Point out each leukocyte.
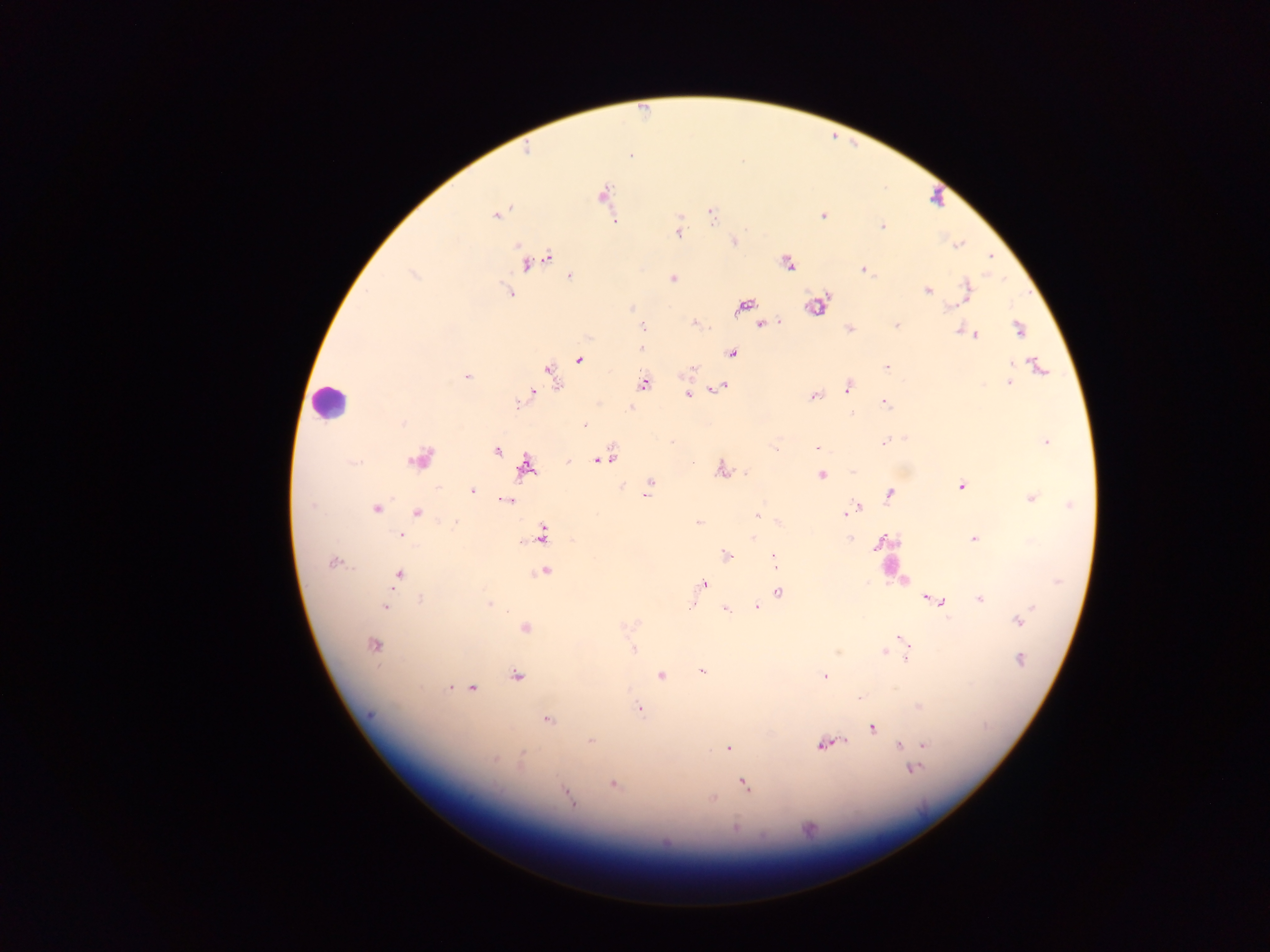
Approximate centers as [x, y] in pixels.
Leukocytes: [328, 403].

field of view = single
image size = 1270×952 pixels
capture = mobile-phone photograph through a microscope
malaria parasite locations = approximate centers as [x, y] in pixels: [630, 154], [603, 195], [711, 214], [821, 215], [496, 217], [679, 221], [882, 226], [677, 230], [734, 242], [548, 258], [787, 262], [526, 266], [863, 270], [569, 275], [672, 278], [506, 284], [966, 284], [928, 291], [510, 292], [967, 296], [963, 300], [948, 304], [631, 306], [781, 320], [693, 322], [643, 325], [760, 325], [896, 325], [849, 328], [961, 328], [1017, 328], [976, 336], [641, 348], [733, 354], [579, 359], [1012, 364], [1036, 366], [885, 367], [694, 370], [549, 371], [467, 376], [644, 384], [1009, 384], [723, 386], [982, 386], [713, 390], [846, 390], [534, 392], [688, 393], [813, 396], [884, 403], [517, 404], [630, 408], [402, 424], [583, 424], [905, 438], [884, 440], [1044, 440], [672, 441], [817, 448], [498, 452], [610, 457], [419, 458], [599, 458], [566, 463], [691, 463], [527, 468], [722, 468], [851, 471], [820, 474], [650, 484], [961, 485], [623, 486], [471, 491], [888, 493], [646, 494], [1031, 497], [507, 501], [1071, 505], [859, 507], [376, 509], [851, 509], [756, 513], [418, 514], [845, 515], [454, 521], [697, 521], [544, 534], [401, 535], [751, 536], [849, 537], [972, 538], [881, 540], [520, 542], [725, 555], [331, 563], [774, 563], [545, 572], [401, 574], [704, 582], [778, 591], [420, 598], [924, 598], [979, 598], [942, 603], [488, 605], [693, 605], [385, 608], [756, 608], [725, 609], [1018, 622], [623, 626], [526, 628], [900, 638], [904, 642], [372, 644], [633, 648], [907, 659], [1020, 659], [703, 672], [660, 676], [516, 677], [823, 677], [449, 686], [473, 688], [895, 688], [860, 697], [916, 706], [640, 708], [547, 721], [872, 728], [591, 742], [844, 742], [819, 744], [924, 744], [898, 745], [727, 750], [522, 759], [496, 760], [911, 762], [744, 785], [612, 786], [563, 789], [712, 798], [570, 799], [735, 827]
preparation = thick blood smear
country = Ghana